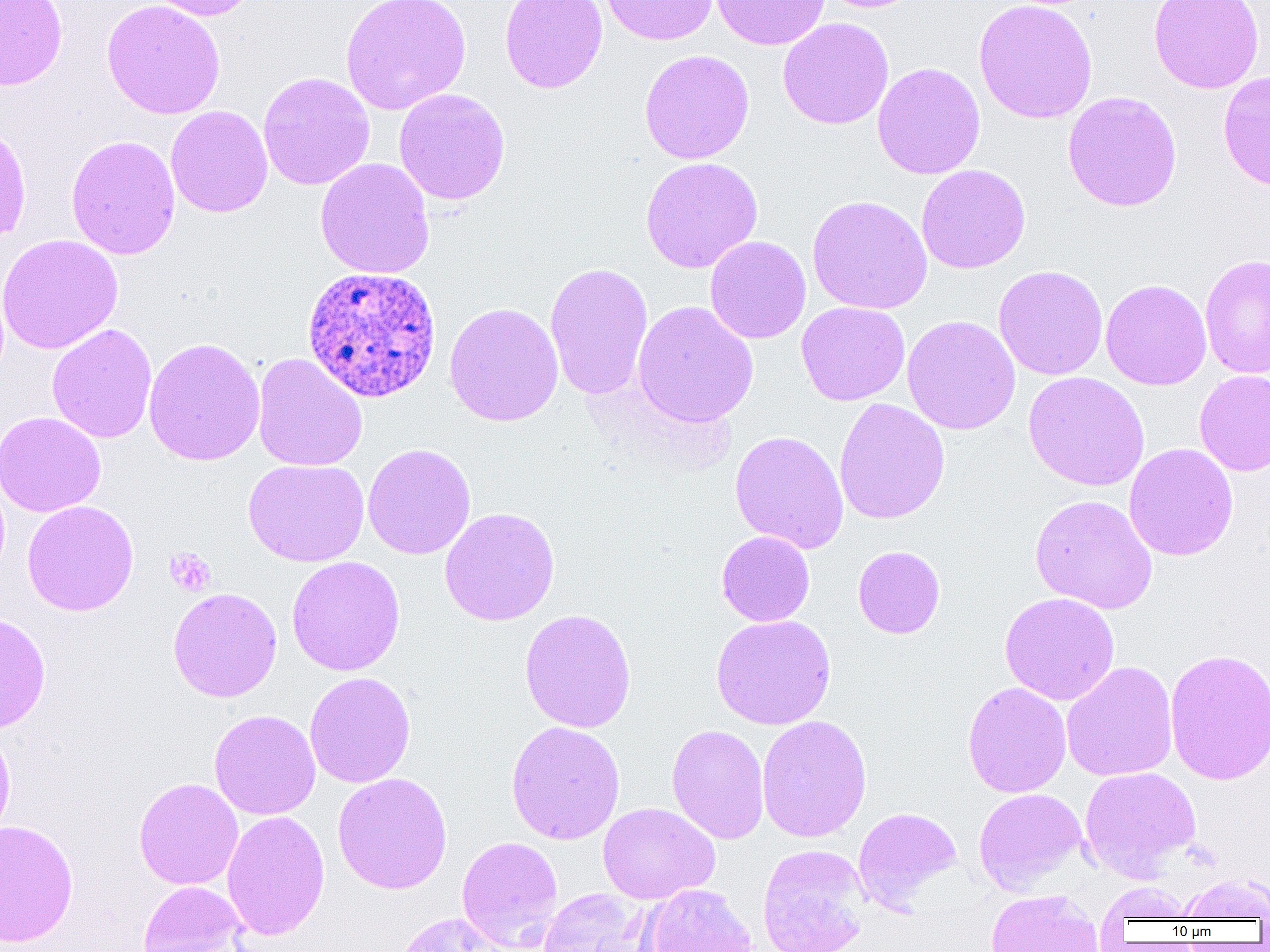

Summary:
  - Coordinate format: approximate bounding boxes as (x1,y1)-(x2,y2) corner pairs in pixels
  - Plasmodium ovale-infected red blood cell locations: (301,265)-(442,403)
  - Platelet locations: (164,547)-(215,596)
  - Uninfected red blood cell locations: (0,0)-(67,91), (101,0)-(225,120), (143,0)-(262,21), (341,0)-(472,115), (500,0)-(607,93), (601,0)-(718,46), (711,0)-(830,50), (814,0)-(925,13), (974,0)-(1097,123), (1148,0)-(1264,93), (777,17)-(894,129), (639,49)-(755,164), (872,62)-(985,179), (1218,69)-(1270,193), (258,72)-(375,190), (393,88)-(511,206), (1062,91)-(1182,212), (165,106)-(273,218), (0,122)-(32,246), (66,135)-(181,260), (315,157)-(435,280), (640,157)-(763,273), (916,164)-(1030,274), (806,195)-(932,315), (0,234)-(123,355), (704,236)-(811,344), (1199,253)-(1270,379), (544,262)-(653,399), (993,265)-(1108,380), (1100,279)-(1212,390), (632,300)-(759,428), (444,301)-(564,427), (796,301)-(910,406), (902,315)-(1021,435), (47,323)-(157,444), (143,337)-(265,466), (252,352)-(367,472), (1194,370)-(1270,476), (1023,371)-(1149,492), (833,397)-(950,525), (0,411)-(106,517), (730,430)-(849,554), (362,443)-(476,560), (1124,443)-(1238,561), (243,458)-(369,567), (1029,494)-(1158,614), (22,500)-(139,616), (439,507)-(560,626), (716,531)-(815,626), (853,545)-(946,639), (287,555)-(405,676), (167,587)-(282,702), (999,592)-(1120,705), (519,608)-(637,733), (0,612)-(51,734), (710,614)-(836,730), (1165,647)-(1270,786), (1061,661)-(1178,781), (304,671)-(416,788), (962,682)-(1072,798), (209,709)-(321,820), (756,714)-(872,843), (505,720)-(626,845), (0,722)-(16,847), (666,724)-(770,845), (1079,766)-(1201,880), (332,772)-(453,895), (133,777)-(244,890), (973,788)-(1087,894), (598,802)-(719,904), (853,807)-(962,912), (222,810)-(330,941), (0,819)-(79,947), (456,836)-(564,951), (757,843)-(872,952), (1174,872)-(1269,921), (137,880)-(250,952), (1094,882)-(1197,927), (638,883)-(759,952), (538,888)-(650,952), (985,889)-(1104,952), (393,912)-(510,952)
  - Slide-level diagnosis: Plasmodium ovale
  - Field of view: single
  - Image size: 1270×952 pixels
  - Magnification: 1000x
  - Modality: optical microscopy
  - Preparation: thin blood smear